Assess for Plasmodium parasites.
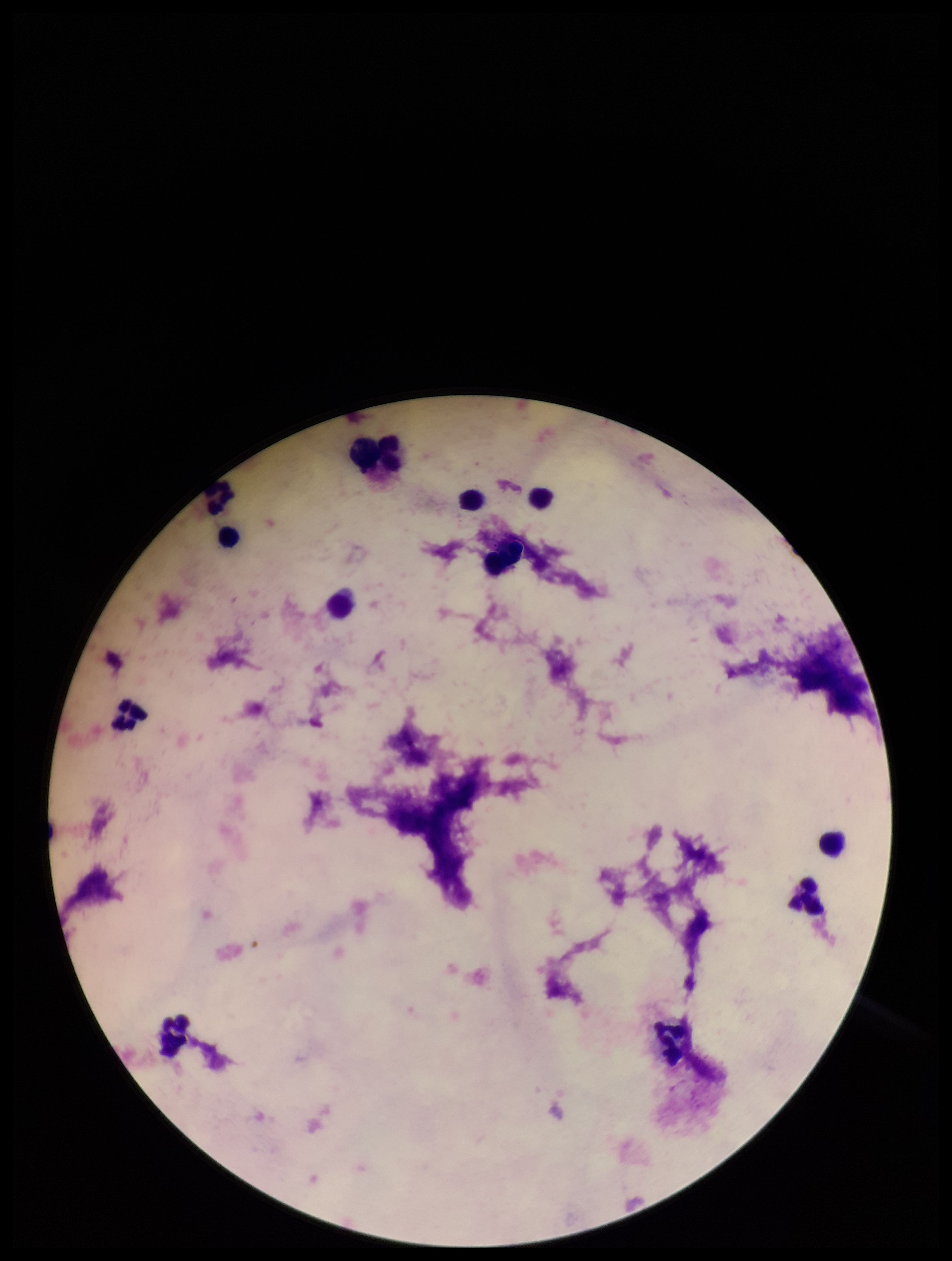
None detected.

Patient malaria status: negative. One field from this slide. Parasite count: 0. Giemsa stain. Image is 952×1261 pixels. Preparation: thick blood smear. Photographed through the microscope eyepiece with a smartphone camera. Leukocyte count: 13.